Name the parasite shown.
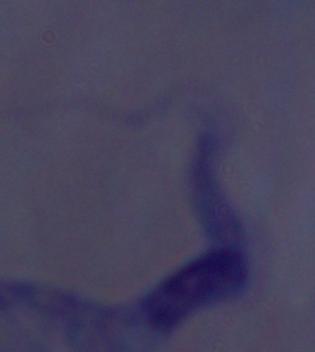
A trypanosome.

Photomicrograph. Captured at 1000x magnification.